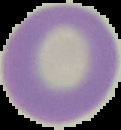

Segmented cell region on a black background. From a thin blood film. Image is 121×130 pixels. Malaria status: uninfected.